Assess this cell for malaria.
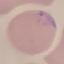

Parasitized.

Acquired by smartphone through the microscope eyepiece. Giemsa-stained preparation. Cell patch, automatically extracted from a larger field of view and resized to 64 × 64 pixels. Thin blood smear.